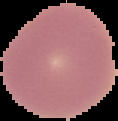

Malaria status: uninfected. Image is 118×121 pixels. The area outside the segmented cell region is set to black. From a thin blood smear.